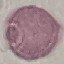 Result: no malaria parasites seen. Thin blood smear. Photographed with a smartphone camera at the microscope eyepiece. Automatically extracted cell patch, resized to 64 × 64 pixels. Giemsa stain.